Assess this cell for malaria.
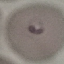

Parasitized.

preparation = thin blood film
capture = smartphone through the microscope eyepiece
stain = Giemsa
image type = cell patch, automatically extracted from a larger field of view and resized to 64 × 64 pixels